Outline each blood parasite and name the species.
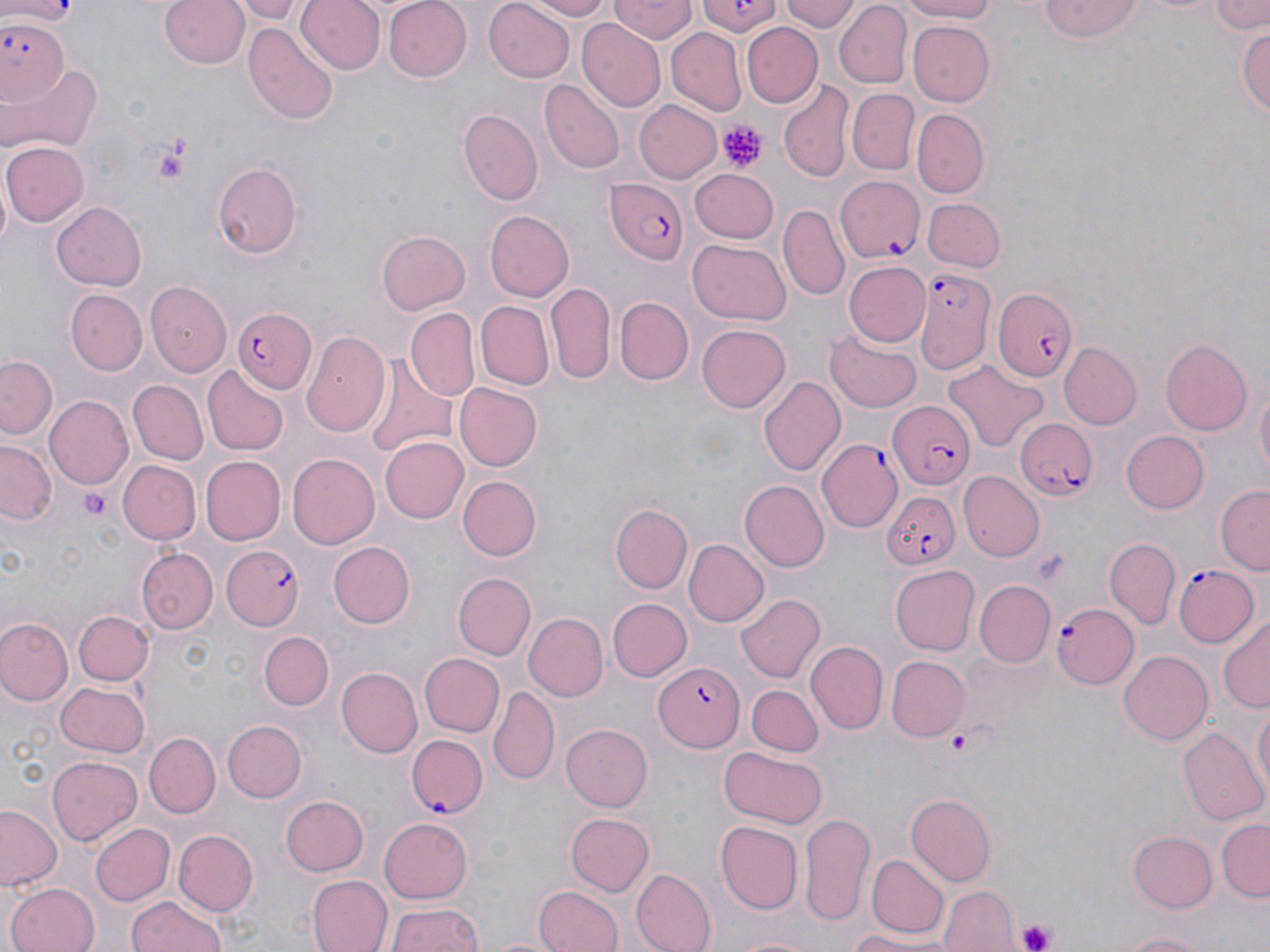

Approximate bounding boxes as (x1, y1, x2, y2) in pixels.
Plasmodium falciparum-infected red blood cells: (0, 17, 68, 107), (834, 175, 926, 262), (605, 177, 688, 266), (918, 266, 996, 382), (993, 285, 1079, 382), (235, 306, 317, 392), (887, 402, 976, 488), (1013, 414, 1098, 502), (819, 439, 905, 533), (882, 488, 958, 569), (220, 545, 304, 631), (1172, 563, 1259, 646), (1051, 602, 1141, 689), (653, 662, 745, 752), (408, 732, 489, 815).
No Plasmodium ovale, Plasmodium malariae, Plasmodium vivax, Babesia divergens, or Trypanosoma brucei observed.

Summary:
  - Platelet locations: (720, 121, 763, 172), (152, 134, 195, 182), (80, 487, 112, 522), (950, 726, 975, 754), (1016, 919, 1056, 952)
  - Uninfected red blood cell locations: (160, 0, 249, 70), (234, 0, 308, 23), (297, 0, 386, 76), (381, 0, 472, 83), (484, 0, 576, 83), (520, 0, 613, 20), (611, 0, 697, 44), (702, 0, 778, 37), (779, 0, 858, 32), (894, 0, 1005, 23), (1037, 0, 1147, 44), (1207, 0, 1267, 33), (834, 2, 911, 85), (579, 21, 665, 111), (907, 21, 997, 104), (245, 24, 339, 127), (1239, 24, 1270, 118), (743, 25, 822, 107), (666, 28, 747, 116), (4, 62, 101, 156), (778, 80, 853, 182), (541, 81, 624, 175), (847, 87, 919, 174), (633, 99, 723, 184), (914, 107, 989, 198), (458, 110, 543, 206), (2, 140, 88, 226), (211, 161, 304, 259), (690, 169, 780, 245), (921, 198, 1004, 273), (50, 201, 147, 292), (778, 204, 850, 301), (486, 210, 574, 301), (376, 229, 471, 314), (687, 238, 793, 326), (844, 262, 930, 346), (545, 281, 615, 383), (145, 282, 232, 377), (66, 290, 146, 375), (616, 297, 693, 385), (474, 301, 554, 390), (405, 309, 479, 399), (697, 325, 792, 412), (827, 327, 924, 411), (301, 330, 390, 434), (1161, 337, 1255, 435), (1060, 342, 1142, 427), (360, 351, 459, 461), (1, 354, 60, 441), (944, 360, 1046, 452), (203, 367, 288, 454), (1251, 371, 1269, 484), (758, 375, 845, 477), (127, 380, 208, 465), (454, 381, 542, 470), (44, 396, 132, 491), (1120, 430, 1209, 514), (0, 438, 60, 526), (380, 438, 468, 523), (286, 453, 378, 549), (200, 456, 284, 546), (117, 460, 199, 544), (962, 470, 1044, 560), (457, 475, 543, 561), (740, 480, 828, 570), (1214, 485, 1270, 573), (617, 498, 718, 646), (613, 503, 693, 593), (683, 538, 768, 627), (1104, 539, 1180, 629), (328, 540, 415, 627), (137, 548, 217, 634), (891, 563, 980, 655), (453, 573, 536, 660), (975, 581, 1054, 665), (737, 594, 827, 682), (605, 598, 691, 681), (73, 610, 154, 686), (524, 612, 607, 701), (1219, 614, 1270, 715), (0, 616, 74, 706), (259, 631, 333, 709), (808, 640, 888, 734), (1118, 648, 1212, 741), (420, 654, 504, 737), (885, 655, 968, 742), (336, 667, 423, 757), (56, 681, 151, 758), (747, 685, 824, 756), (489, 686, 559, 785), (1252, 701, 1269, 799), (220, 720, 304, 804), (561, 723, 654, 810), (1178, 724, 1268, 826), (144, 731, 221, 816), (720, 745, 825, 827), (47, 755, 140, 844), (906, 794, 997, 884), (279, 795, 369, 876), (0, 804, 64, 890), (799, 811, 877, 923), (564, 812, 653, 898), (379, 818, 474, 902), (1217, 818, 1269, 900), (715, 821, 803, 914), (89, 822, 175, 906), (172, 829, 258, 917), (1128, 831, 1218, 912), (870, 853, 947, 936), (630, 868, 717, 952), (308, 874, 391, 952), (6, 882, 101, 952), (534, 885, 622, 952), (939, 885, 1019, 952), (126, 896, 228, 952), (387, 903, 485, 952), (846, 929, 944, 951), (1118, 929, 1216, 952), (731, 933, 815, 952)
  - Slide-level diagnosis: Plasmodium falciparum
  - Field of view: one of a larger specimen
  - Stain: May-Grünwald-Giemsa
  - Modality: optical microscopy
  - Magnification: 1000x
  - Preparation: thin blood smear
  - Image size: 1270×952 pixels